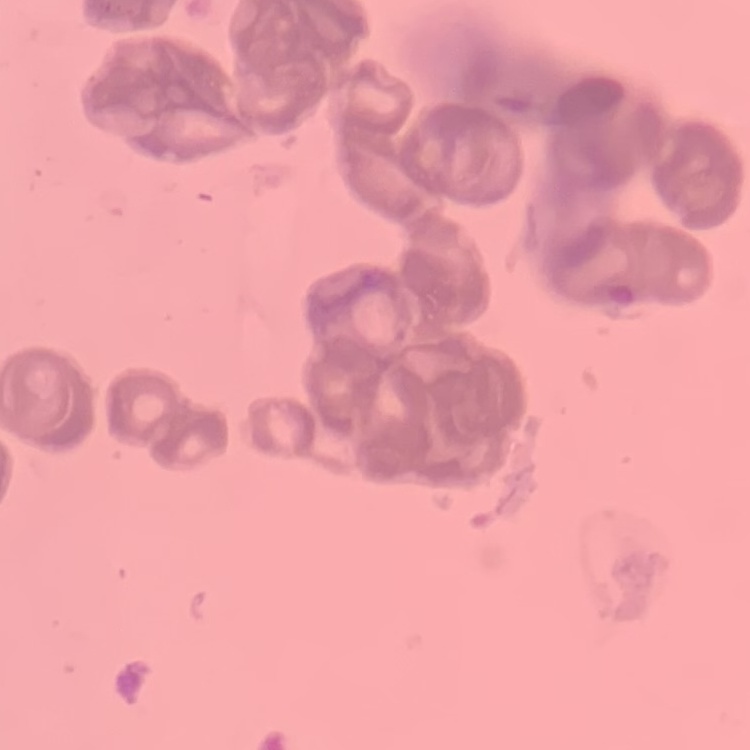 The red blood cells show rouleaux formation. One tile cut from a larger photomicrograph. Field's or Giemsa stain. Thin blood film.